Give the extent of all Trypanosoma brucei.
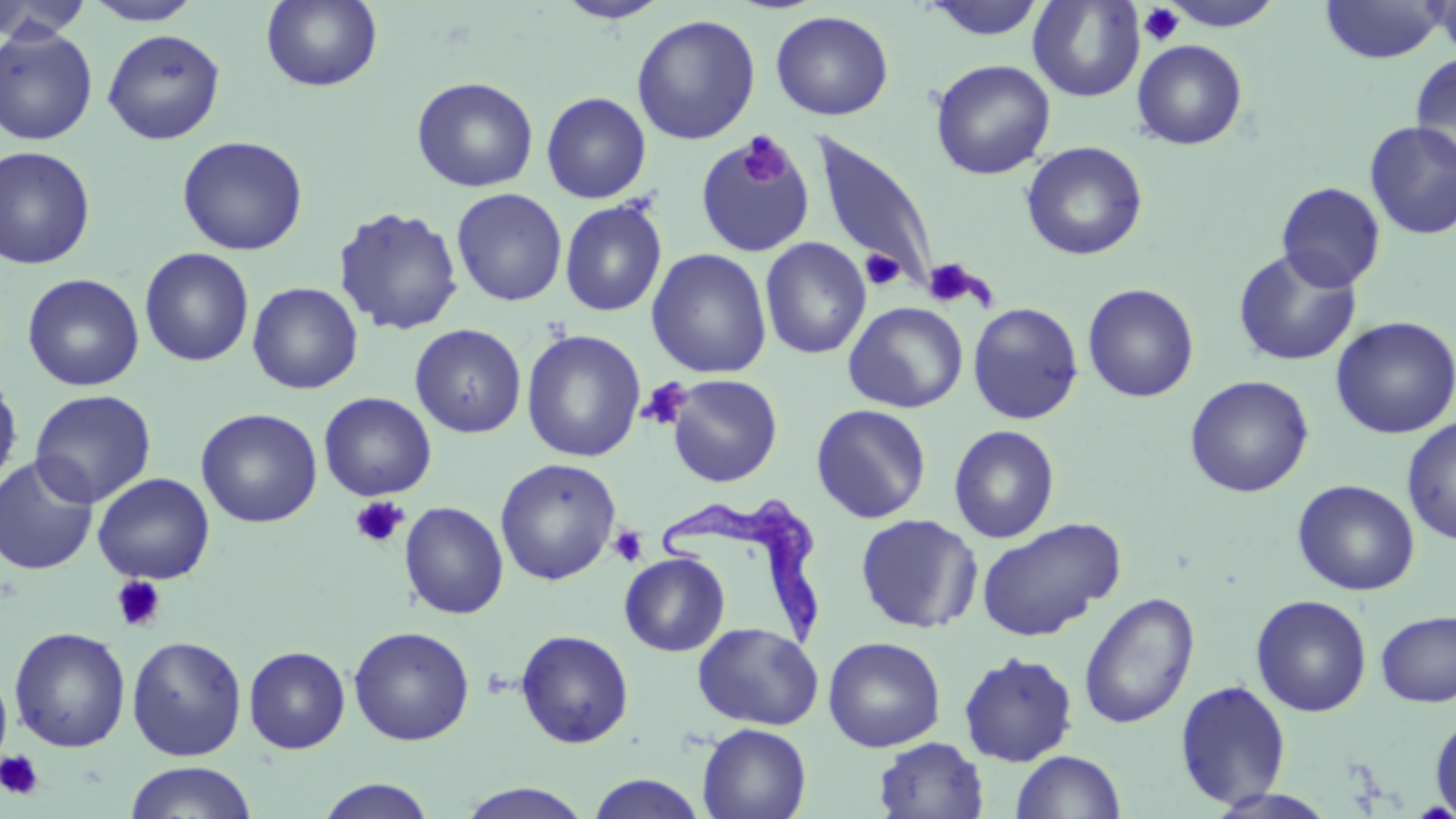
Approximate bounding boxes as named x1/y1/x2/y2 corners in pixels.
Trypanosoma brucei: (x1=657, y1=493, x2=824, y2=653).

slide-level diagnosis = Trypanosoma brucei
preparation = thin blood smear
field of view = one of a larger specimen
platelet locations = approximate bounding boxes as named x1/y1/x2/y2 corners in pixels: (x1=1138, y1=3, x2=1186, y2=47), (x1=738, y1=134, x2=790, y2=187), (x1=860, y1=249, x2=905, y2=291), (x1=922, y1=257, x2=987, y2=309), (x1=638, y1=379, x2=691, y2=430), (x1=350, y1=496, x2=409, y2=549), (x1=608, y1=525, x2=648, y2=567), (x1=110, y1=575, x2=167, y2=632), (x1=0, y1=749, x2=44, y2=800)
uninfected red blood cell locations = approximate bounding boxes as named x1/y1/x2/y2 corners in pixels: (x1=0, y1=0, x2=93, y2=43), (x1=82, y1=0, x2=203, y2=25), (x1=260, y1=0, x2=383, y2=92), (x1=921, y1=0, x2=1049, y2=41), (x1=1028, y1=0, x2=1144, y2=102), (x1=1160, y1=0, x2=1285, y2=31), (x1=1432, y1=0, x2=1456, y2=62), (x1=554, y1=1, x2=671, y2=23), (x1=1319, y1=1, x2=1448, y2=64), (x1=770, y1=10, x2=894, y2=121), (x1=631, y1=14, x2=761, y2=145), (x1=0, y1=25, x2=98, y2=145), (x1=103, y1=28, x2=226, y2=145), (x1=1132, y1=39, x2=1248, y2=151), (x1=1409, y1=51, x2=1456, y2=173), (x1=930, y1=59, x2=1055, y2=180), (x1=411, y1=76, x2=539, y2=193), (x1=541, y1=91, x2=652, y2=204), (x1=1364, y1=121, x2=1456, y2=240), (x1=695, y1=133, x2=815, y2=258), (x1=811, y1=133, x2=940, y2=292), (x1=176, y1=135, x2=308, y2=255), (x1=1021, y1=141, x2=1148, y2=261), (x1=0, y1=145, x2=96, y2=270), (x1=1276, y1=182, x2=1386, y2=292), (x1=451, y1=188, x2=568, y2=306), (x1=559, y1=198, x2=667, y2=317), (x1=333, y1=205, x2=465, y2=336), (x1=761, y1=237, x2=870, y2=359), (x1=139, y1=247, x2=254, y2=367), (x1=647, y1=248, x2=772, y2=379), (x1=1232, y1=248, x2=1362, y2=367), (x1=22, y1=273, x2=145, y2=392), (x1=247, y1=282, x2=363, y2=394), (x1=1082, y1=283, x2=1199, y2=403), (x1=844, y1=301, x2=968, y2=413), (x1=968, y1=302, x2=1083, y2=425), (x1=1330, y1=316, x2=1456, y2=439), (x1=410, y1=323, x2=526, y2=438), (x1=521, y1=329, x2=646, y2=462), (x1=0, y1=374, x2=23, y2=490), (x1=666, y1=374, x2=782, y2=487), (x1=1185, y1=375, x2=1314, y2=498), (x1=30, y1=389, x2=156, y2=507), (x1=319, y1=392, x2=437, y2=501), (x1=810, y1=404, x2=931, y2=523), (x1=195, y1=408, x2=323, y2=528), (x1=1402, y1=416, x2=1456, y2=545), (x1=949, y1=425, x2=1060, y2=544), (x1=0, y1=456, x2=99, y2=575), (x1=495, y1=458, x2=621, y2=585), (x1=93, y1=472, x2=215, y2=584), (x1=1293, y1=479, x2=1420, y2=596), (x1=399, y1=501, x2=508, y2=619), (x1=856, y1=514, x2=982, y2=633), (x1=976, y1=518, x2=1125, y2=642), (x1=619, y1=552, x2=730, y2=656), (x1=1079, y1=592, x2=1199, y2=729), (x1=1250, y1=594, x2=1372, y2=717), (x1=1375, y1=609, x2=1456, y2=707), (x1=693, y1=622, x2=823, y2=730), (x1=349, y1=625, x2=475, y2=746), (x1=9, y1=626, x2=130, y2=752), (x1=515, y1=629, x2=634, y2=748), (x1=126, y1=635, x2=248, y2=761), (x1=823, y1=636, x2=946, y2=752), (x1=243, y1=646, x2=351, y2=754), (x1=958, y1=651, x2=1078, y2=766), (x1=0, y1=662, x2=13, y2=778), (x1=1174, y1=679, x2=1292, y2=809), (x1=1429, y1=712, x2=1456, y2=817), (x1=697, y1=723, x2=811, y2=819), (x1=873, y1=736, x2=989, y2=819), (x1=1011, y1=750, x2=1126, y2=819), (x1=124, y1=761, x2=258, y2=819), (x1=585, y1=774, x2=709, y2=818), (x1=312, y1=778, x2=439, y2=818), (x1=455, y1=782, x2=595, y2=818), (x1=1204, y1=788, x2=1341, y2=819)
stain = May-Grünwald-Giemsa
magnification = 1000x
modality = light microscopy
image size = 1456×819 pixels